Report the malaria status of this cell.
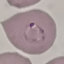

Parasitized.

{
  "image_type": "cell patch, automatically extracted from a larger field of view and resized to 64 × 64 pixels",
  "capture": "smartphone through the microscope eyepiece",
  "stain": "Giemsa",
  "preparation": "thin blood smear"
}